Locate and identify every blood parasite.
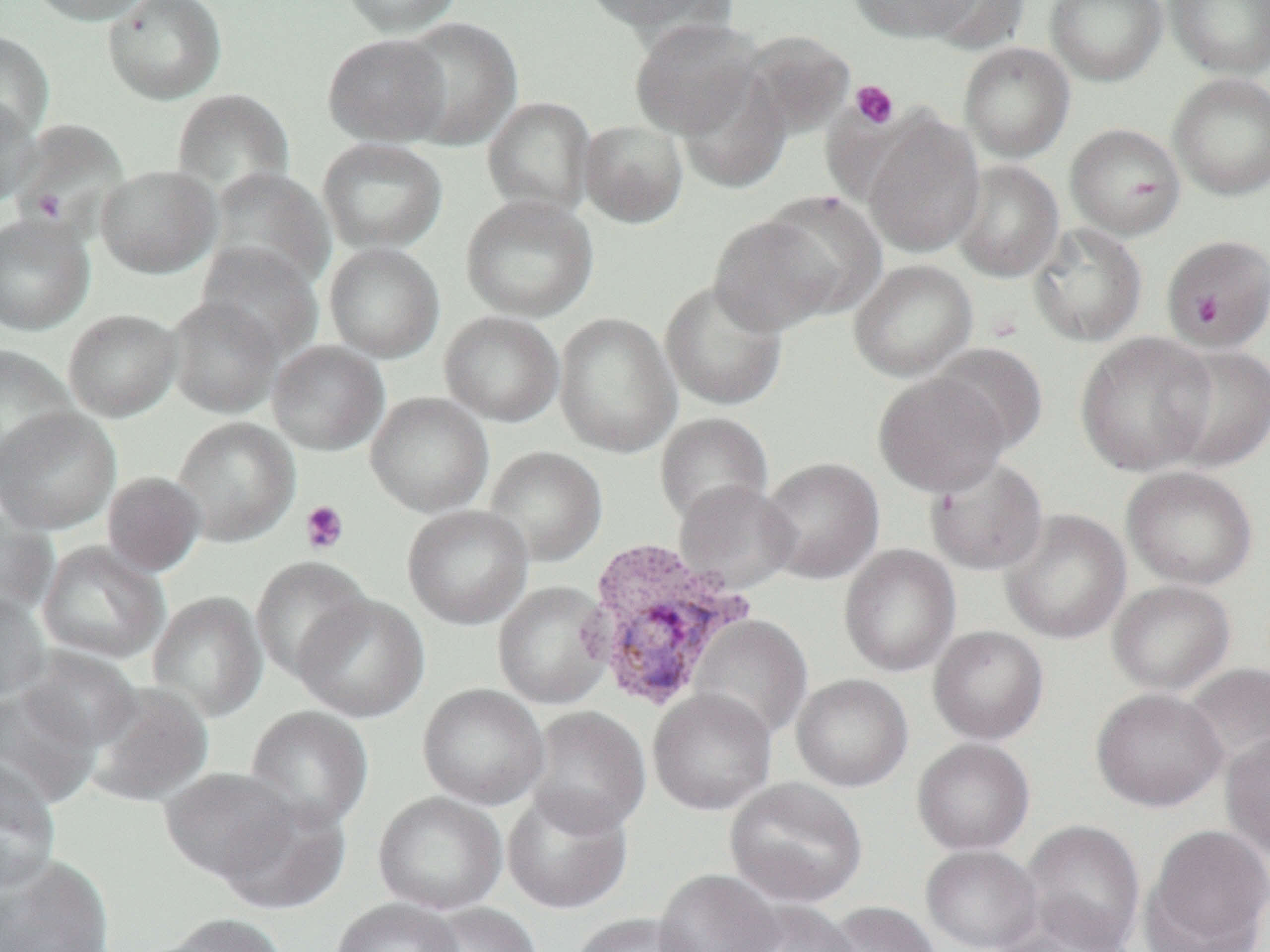

Approximate bounding boxes as named x1/y1/x2/y2 corners in pixels.
Plasmodium vivax-infected red blood cells: (x1=579, y1=536, x2=755, y2=713).
No Plasmodium falciparum, Plasmodium ovale, Plasmodium malariae, Babesia divergens, or Trypanosoma brucei observed.

Uninfected red blood cell locations: (x1=28, y1=0, x2=154, y2=25), (x1=103, y1=0, x2=227, y2=105), (x1=338, y1=0, x2=465, y2=37), (x1=581, y1=0, x2=735, y2=37), (x1=849, y1=0, x2=986, y2=43), (x1=920, y1=0, x2=1032, y2=53), (x1=1045, y1=0, x2=1168, y2=86), (x1=1165, y1=0, x2=1270, y2=79), (x1=395, y1=17, x2=523, y2=149), (x1=630, y1=18, x2=761, y2=139), (x1=739, y1=30, x2=856, y2=139), (x1=0, y1=31, x2=55, y2=143), (x1=323, y1=33, x2=451, y2=146), (x1=958, y1=42, x2=1075, y2=162), (x1=676, y1=70, x2=791, y2=194), (x1=1167, y1=72, x2=1270, y2=201), (x1=171, y1=88, x2=295, y2=200), (x1=482, y1=96, x2=596, y2=217), (x1=0, y1=97, x2=41, y2=206), (x1=861, y1=114, x2=985, y2=258), (x1=10, y1=119, x2=130, y2=236), (x1=578, y1=119, x2=689, y2=228), (x1=1065, y1=122, x2=1186, y2=240), (x1=317, y1=137, x2=448, y2=254), (x1=951, y1=159, x2=1064, y2=283), (x1=96, y1=165, x2=220, y2=278), (x1=204, y1=167, x2=334, y2=292), (x1=460, y1=194, x2=599, y2=321), (x1=709, y1=211, x2=846, y2=335), (x1=0, y1=213, x2=96, y2=335), (x1=1028, y1=222, x2=1148, y2=347), (x1=1160, y1=233, x2=1270, y2=352), (x1=324, y1=242, x2=445, y2=362), (x1=195, y1=244, x2=323, y2=363), (x1=848, y1=259, x2=978, y2=382), (x1=660, y1=278, x2=788, y2=411), (x1=166, y1=296, x2=284, y2=418), (x1=63, y1=308, x2=182, y2=422), (x1=439, y1=311, x2=565, y2=427), (x1=554, y1=312, x2=681, y2=457), (x1=1075, y1=331, x2=1218, y2=476), (x1=267, y1=340, x2=389, y2=456), (x1=930, y1=342, x2=1049, y2=455), (x1=1159, y1=344, x2=1270, y2=472), (x1=0, y1=345, x2=78, y2=475), (x1=873, y1=372, x2=1011, y2=496), (x1=365, y1=392, x2=494, y2=517), (x1=0, y1=407, x2=121, y2=534), (x1=654, y1=412, x2=774, y2=527), (x1=171, y1=416, x2=300, y2=547), (x1=482, y1=446, x2=608, y2=567), (x1=924, y1=456, x2=1048, y2=576), (x1=758, y1=457, x2=885, y2=585), (x1=1121, y1=466, x2=1258, y2=591), (x1=101, y1=471, x2=206, y2=576), (x1=673, y1=481, x2=799, y2=593), (x1=402, y1=504, x2=533, y2=629), (x1=0, y1=508, x2=59, y2=621), (x1=1000, y1=509, x2=1132, y2=644), (x1=37, y1=541, x2=169, y2=665), (x1=839, y1=544, x2=961, y2=677), (x1=251, y1=555, x2=372, y2=682), (x1=1107, y1=580, x2=1236, y2=695), (x1=492, y1=581, x2=614, y2=710), (x1=0, y1=591, x2=50, y2=703), (x1=147, y1=591, x2=268, y2=722), (x1=293, y1=593, x2=430, y2=723), (x1=689, y1=615, x2=813, y2=743), (x1=928, y1=625, x2=1049, y2=745), (x1=16, y1=646, x2=143, y2=751), (x1=1180, y1=662, x2=1270, y2=774), (x1=791, y1=674, x2=913, y2=792), (x1=84, y1=682, x2=214, y2=807), (x1=417, y1=683, x2=550, y2=810), (x1=1, y1=687, x2=101, y2=808), (x1=1091, y1=687, x2=1228, y2=812), (x1=648, y1=689, x2=776, y2=815), (x1=245, y1=705, x2=373, y2=832), (x1=524, y1=706, x2=651, y2=836), (x1=1221, y1=732, x2=1270, y2=858), (x1=911, y1=738, x2=1035, y2=855), (x1=0, y1=758, x2=61, y2=893), (x1=159, y1=767, x2=297, y2=882), (x1=725, y1=777, x2=867, y2=907), (x1=502, y1=787, x2=633, y2=915), (x1=373, y1=791, x2=507, y2=915), (x1=214, y1=796, x2=351, y2=916), (x1=1021, y1=819, x2=1146, y2=952), (x1=1144, y1=823, x2=1270, y2=951), (x1=920, y1=844, x2=1043, y2=952), (x1=0, y1=854, x2=115, y2=951), (x1=654, y1=869, x2=784, y2=952), (x1=331, y1=897, x2=462, y2=952), (x1=729, y1=900, x2=861, y2=952), (x1=824, y1=901, x2=941, y2=952), (x1=994, y1=901, x2=1134, y2=952), (x1=419, y1=903, x2=543, y2=952), (x1=571, y1=912, x2=700, y2=952), (x1=155, y1=913, x2=292, y2=952). Platelet locations: (x1=850, y1=80, x2=899, y2=129), (x1=33, y1=189, x2=67, y2=222), (x1=1194, y1=292, x2=1225, y2=325), (x1=300, y1=500, x2=350, y2=554). Slide-level diagnosis: Plasmodium vivax. Single field of view. Optical microscopy. 1000x magnification. Thin blood smear. Image is 1270×952 pixels.